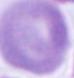

{
  "modality": "photomicrograph",
  "identification": "red blood cell",
  "magnification": "1000x"
}